Report the malaria status of this cell.
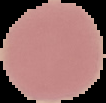

It is uninfected.

preparation = thin blood smear
image type = segmented cell region with the area outside set to black
image size = 106×103 pixels